State which parasite is depicted.
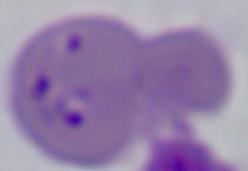

Babesia.

1000x magnification. Photomicrograph.